Locate every Plasmodium parasite and every leukocyte.
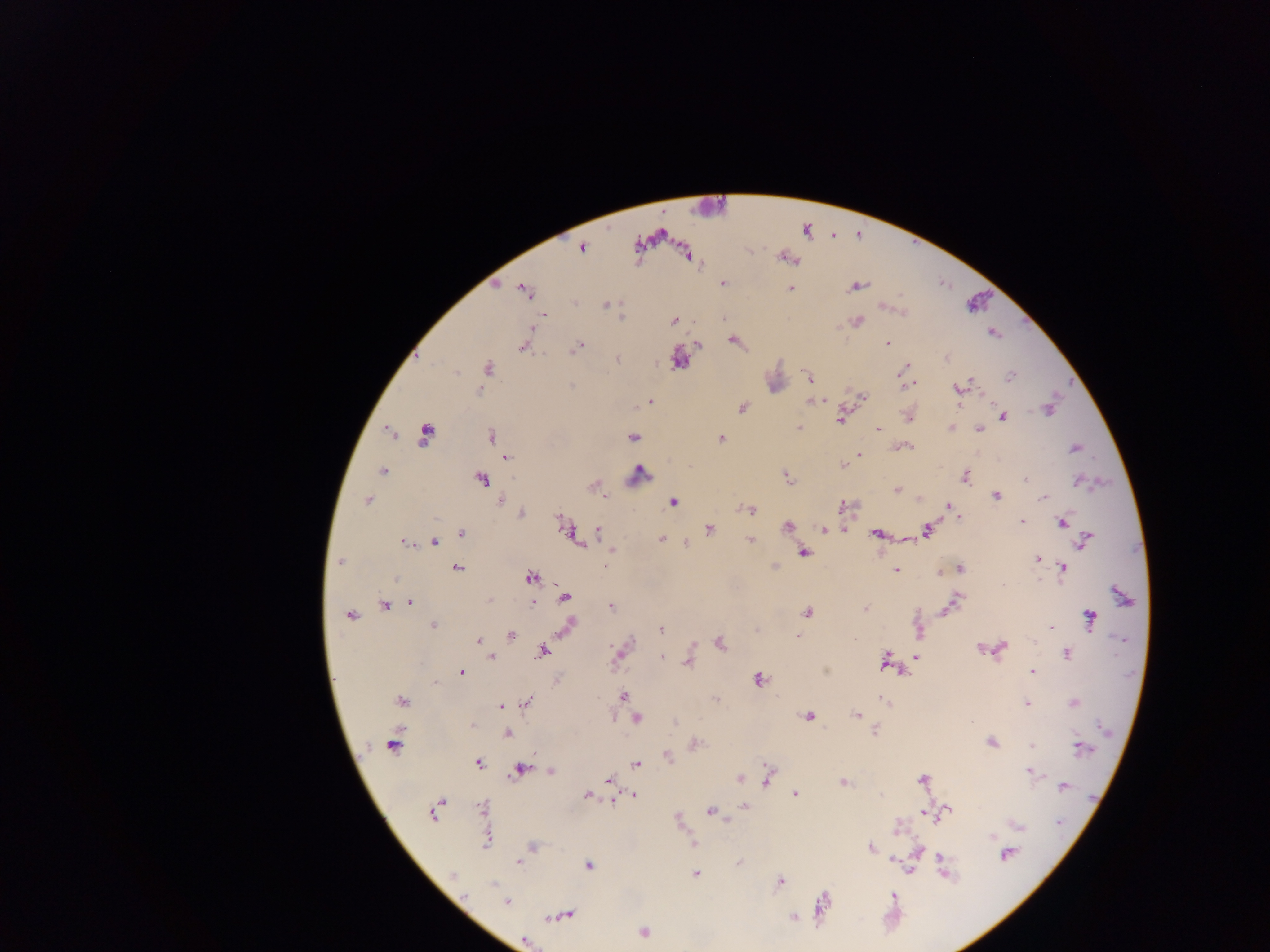

Approximate centers as [x, y] in pixels.
Plasmodium parasites: [639, 248], [582, 249], [723, 282], [852, 287], [789, 288], [524, 289], [606, 306], [880, 306], [544, 314], [540, 315], [674, 319], [722, 320], [858, 321], [531, 329], [992, 333], [733, 340], [885, 343], [699, 344], [582, 345], [522, 346], [578, 347], [617, 358], [947, 360], [907, 365], [486, 369], [902, 373], [808, 376], [1008, 376], [903, 380], [970, 380], [964, 384], [572, 385], [957, 389], [980, 393], [861, 396], [810, 400], [651, 401], [957, 406], [741, 407], [1047, 410], [1033, 411], [1004, 418], [840, 419], [799, 426], [950, 426], [877, 429], [980, 430], [423, 434], [490, 436], [632, 437], [721, 438], [906, 446], [1074, 449], [860, 453], [857, 456], [505, 457], [843, 466], [384, 471], [641, 471], [482, 479], [1026, 480], [1079, 482], [591, 484], [897, 488], [996, 495], [919, 497], [1042, 498], [369, 501], [501, 502], [673, 502], [947, 505], [750, 510], [521, 513], [559, 515], [960, 518], [1021, 519], [1062, 522], [1069, 525], [930, 526], [787, 527], [845, 527], [598, 528], [822, 529], [709, 530], [829, 530], [569, 532], [463, 534], [877, 534], [574, 537], [661, 537], [910, 539], [1086, 539], [751, 540], [434, 542], [405, 543], [686, 543], [803, 552], [1037, 559], [340, 562], [456, 567], [1063, 567], [896, 568], [532, 578], [1061, 582], [563, 597], [957, 598], [489, 601], [411, 602], [533, 603], [385, 607], [611, 607], [865, 607], [807, 612], [350, 615], [1089, 616], [570, 622], [433, 626], [1050, 627], [661, 629], [510, 635], [797, 636], [479, 640], [721, 642], [631, 643], [1005, 646], [691, 648], [979, 648], [618, 650], [1001, 650], [543, 652], [1066, 653], [615, 656], [917, 656], [491, 657], [662, 657], [885, 658], [616, 662], [688, 662], [884, 664], [462, 671], [825, 671], [1033, 672], [759, 679], [623, 695], [402, 701], [526, 703], [1026, 703], [1073, 703], [500, 707], [858, 716], [638, 717], [807, 718], [471, 724], [508, 733], [992, 741], [391, 743], [1077, 743], [1032, 745], [478, 763], [636, 765], [521, 769], [552, 771], [1028, 771], [740, 779], [609, 780], [767, 780], [921, 781], [843, 783], [1064, 787], [632, 795], [796, 795], [587, 797], [613, 800], [745, 806], [948, 809], [433, 812], [709, 812], [924, 813], [727, 820], [1057, 824], [1021, 828], [992, 838], [871, 848], [1013, 853], [1007, 855], [941, 857], [893, 860], [519, 862], [590, 865], [911, 869], [453, 876], [493, 883], [781, 883], [506, 901], [823, 903], [570, 914], [643, 932], [527, 941].
No leukocytes observed.

Mobile-phone photograph taken through the microscope. One field of view. Thick blood smear. Image is 1270×952 pixels. Sample from Ghana.